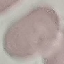

Summary:
  - Result: no malaria parasites seen
  - Image type: cell patch, automatically extracted from a larger field of view and resized to 64 × 64 pixels
  - Preparation: thin blood film
  - Capture: smartphone through the microscope eyepiece
  - Stain: Giemsa